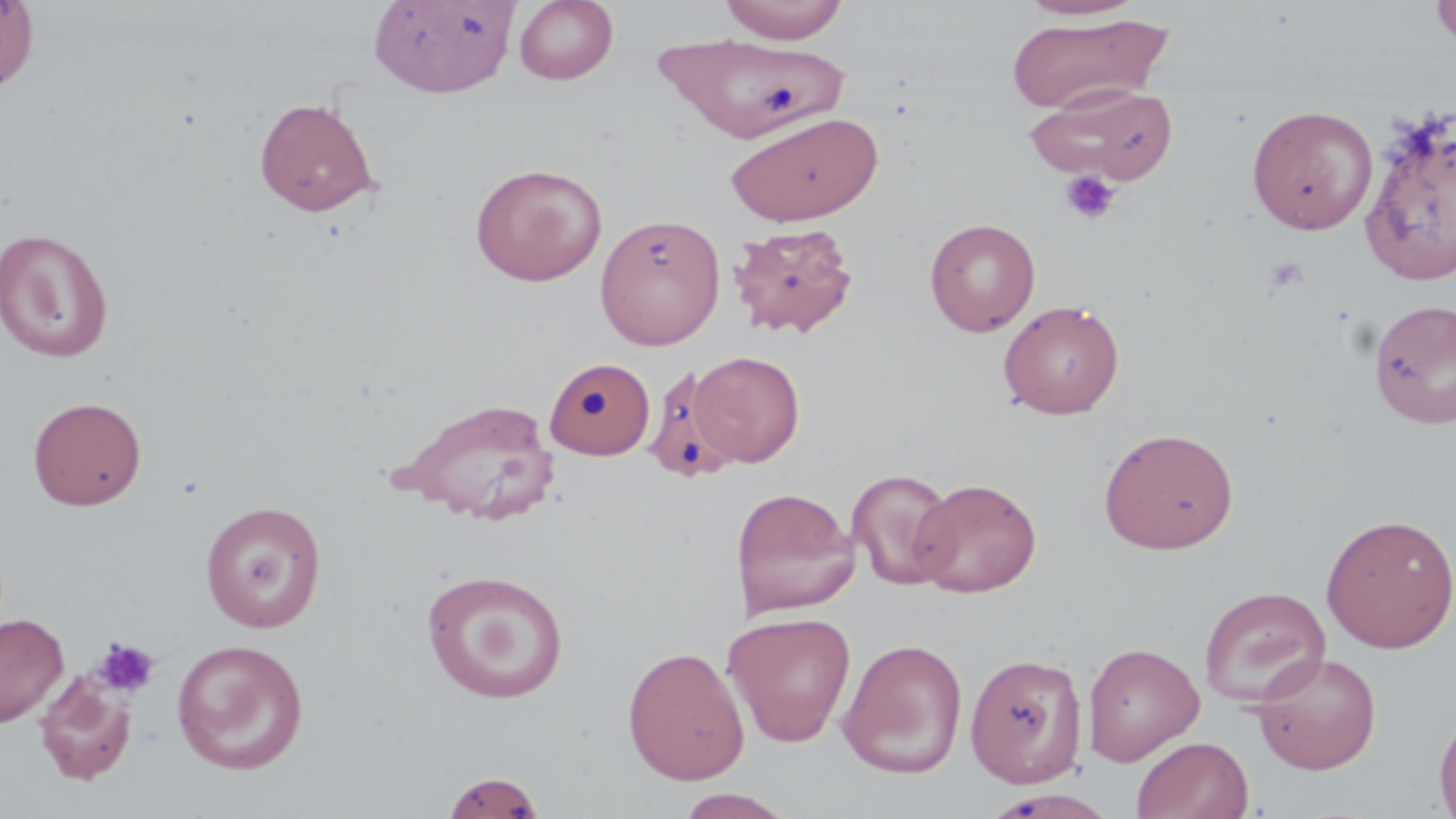

slide-level diagnosis = no evidence of blood parasites
preparation = thin blood film
stain = May-Grünwald-Giemsa
field of view = one of a larger specimen
uninfected red blood cell locations = approximate bounding boxes as [x1, y1, x2, y2] in pixels: [0, 0, 40, 95], [368, 0, 518, 98], [514, 0, 619, 85], [720, 0, 849, 44], [1018, 0, 1142, 21], [1430, 0, 1456, 50], [1005, 13, 1172, 115], [652, 31, 857, 151], [1027, 85, 1178, 185], [254, 96, 380, 217], [1247, 104, 1379, 235], [1359, 110, 1455, 287], [723, 111, 884, 226], [470, 162, 607, 286], [594, 212, 725, 349], [924, 217, 1041, 336], [729, 221, 859, 338], [0, 228, 114, 363], [1368, 297, 1456, 430], [998, 299, 1125, 419], [691, 351, 805, 468], [545, 356, 655, 459], [645, 362, 760, 480], [27, 395, 147, 510], [395, 396, 560, 525], [1099, 426, 1239, 554], [846, 468, 959, 590], [910, 477, 1042, 597], [730, 486, 859, 619], [198, 500, 327, 632], [1320, 513, 1456, 653], [420, 568, 570, 704], [1199, 585, 1331, 708], [723, 611, 857, 747], [0, 613, 69, 728], [837, 637, 969, 779], [171, 638, 309, 774], [1082, 641, 1205, 765], [622, 645, 750, 785], [1250, 651, 1383, 775], [965, 652, 1089, 788], [35, 671, 136, 785], [1433, 708, 1456, 817], [1131, 735, 1254, 819], [441, 769, 547, 818], [673, 789, 797, 818]
platelet locations = approximate bounding boxes as [x1, y1, x2, y2] in pixels: [1059, 170, 1122, 225], [1264, 256, 1309, 295], [92, 636, 160, 698]
modality = light microscopy
image size = 1456×819 pixels
magnification = 1000x